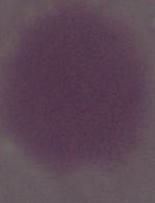
Summary:
  - Modality: photomicrograph
  - Identification: red blood cell
  - Magnification: 1000x